Name the parasite shown.
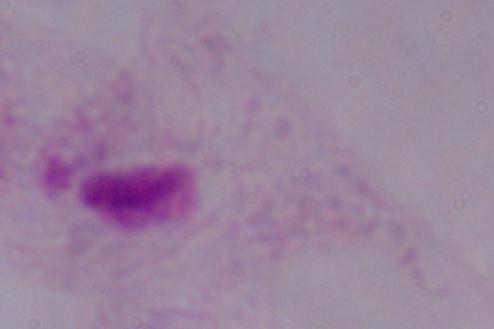

A trichomonad.

Summary:
  - Modality: photomicrograph
  - Magnification: 1000x